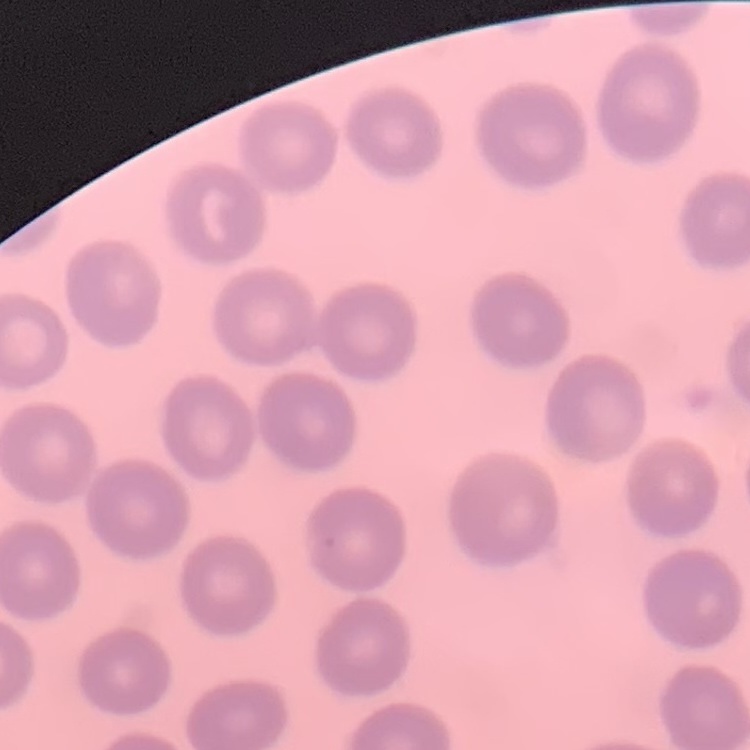

The erythrocytes exhibit no rouleaux formation. Stained with either Field's or Giemsa. One tile cut from a larger photomicrograph. Thin blood smear.